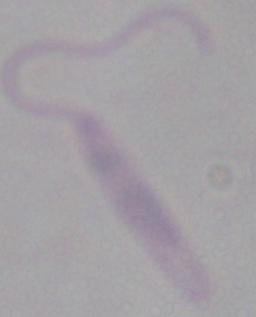

modality = micrograph
identification = Leishmania
magnification = 1000x